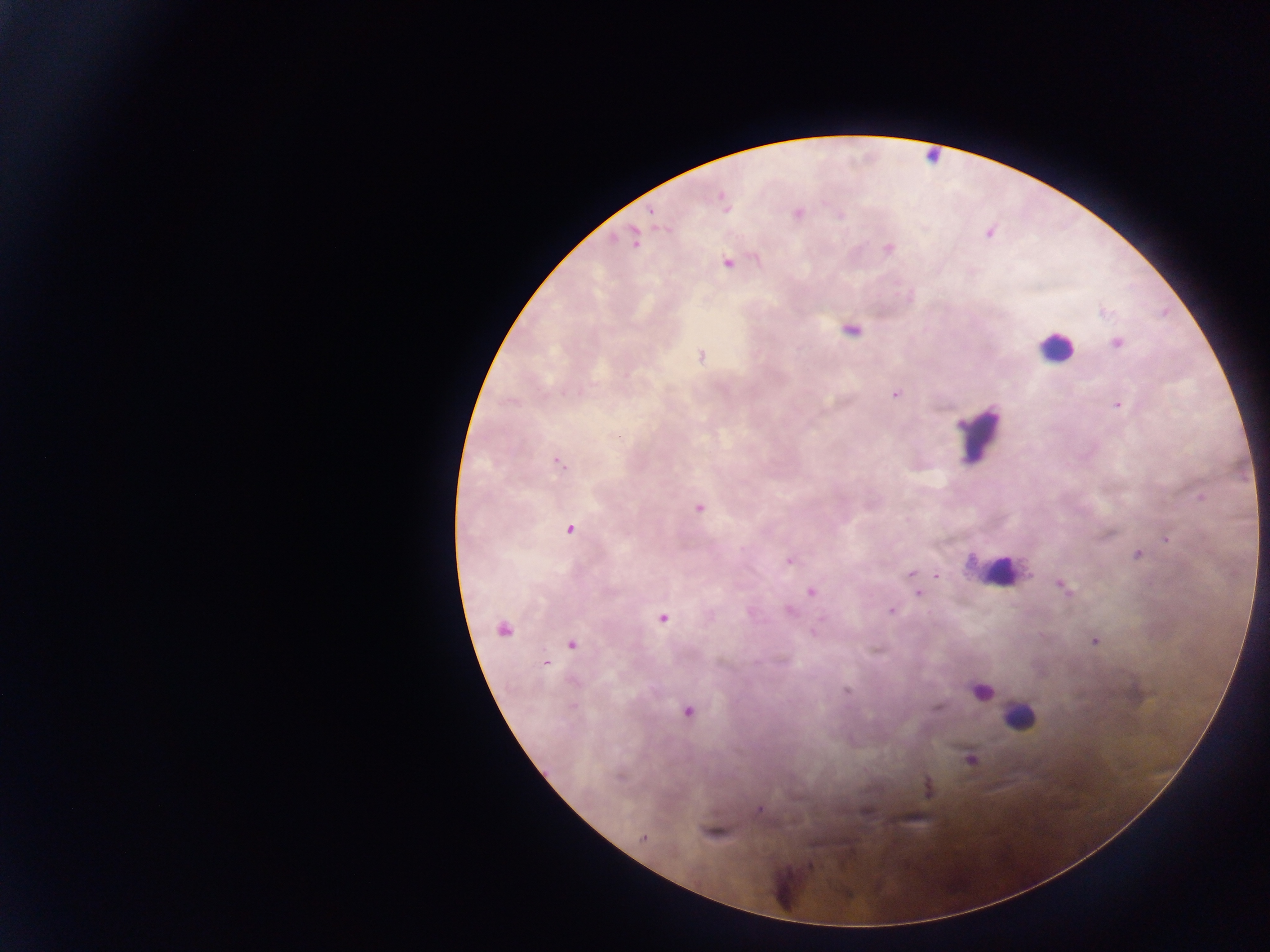 Approximate centers as (x, y) in pixels. Malaria parasite locations: (723, 201), (798, 213), (989, 233), (634, 240), (889, 248), (727, 263), (1103, 312), (852, 331), (1117, 342), (701, 355), (895, 394), (1118, 405), (558, 464), (1201, 498), (699, 508), (569, 529), (1167, 538), (1137, 554), (790, 561), (910, 574), (936, 576), (1063, 587), (811, 592), (919, 594), (891, 611), (663, 618), (503, 630), (1094, 641), (571, 644), (545, 664), (847, 691), (687, 712), (970, 759), (760, 809), (643, 838). Leukocyte locations: (931, 157), (1054, 347), (980, 434), (999, 577), (981, 691), (1019, 716). One field of view. Mobile-phone photograph taken through the microscope. Thick blood film. Collected in Ghana. Image is 1270×952 pixels.